Outline platelets.
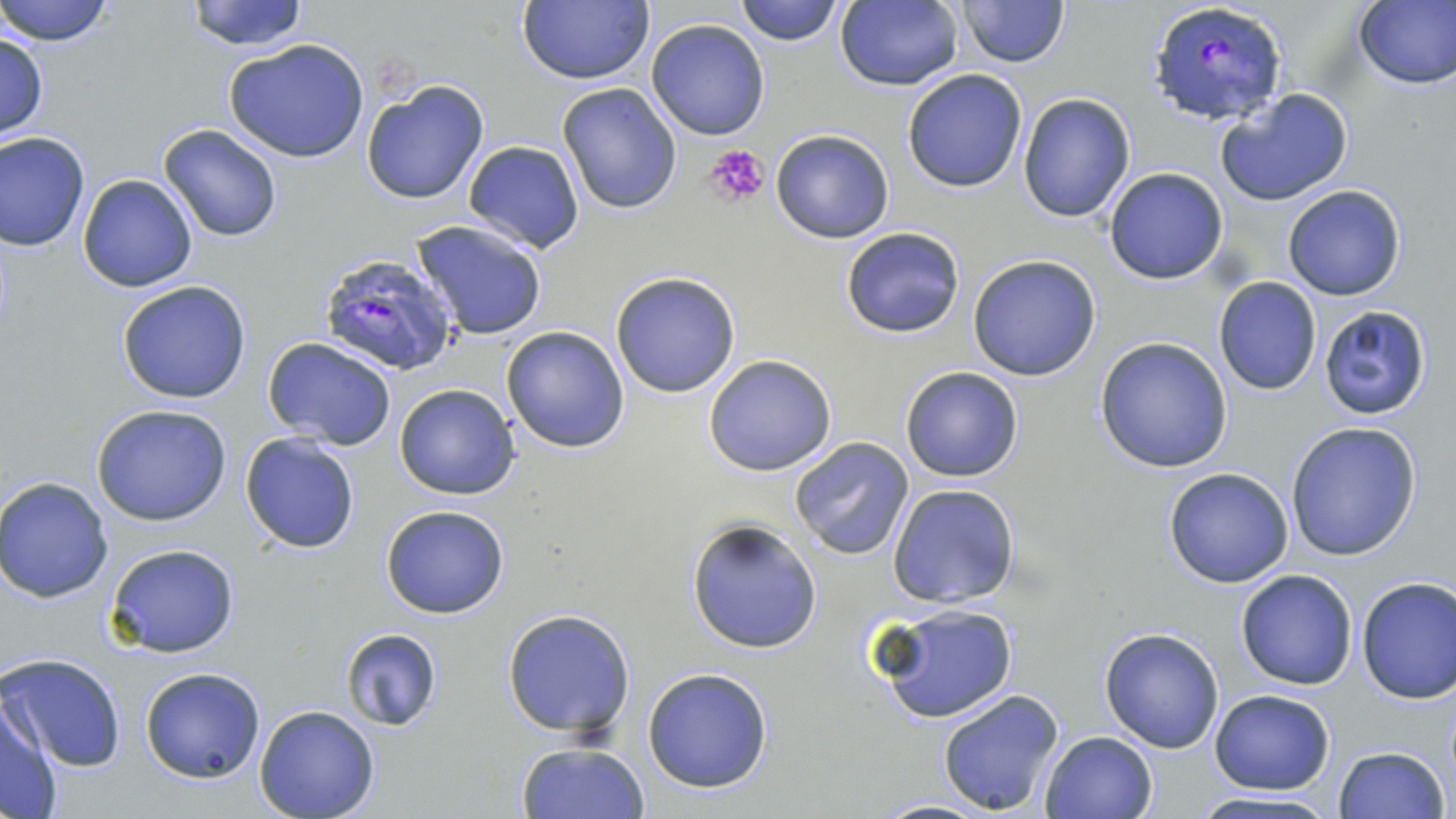

Approximate bounding boxes as [x1, y1, x2, y2] in pixels.
Platelets: [705, 143, 770, 208].

Summary:
  - Uninfected red blood cell locations: [0, 0, 117, 47], [186, 0, 310, 51], [520, 0, 655, 85], [732, 0, 846, 46], [835, 0, 964, 91], [956, 0, 1070, 68], [1353, 1, 1456, 90], [645, 19, 770, 140], [0, 32, 48, 142], [224, 38, 370, 163], [901, 68, 1028, 192], [360, 80, 489, 206], [556, 82, 684, 216], [1215, 88, 1355, 207], [1018, 92, 1136, 223], [158, 124, 283, 242], [769, 128, 895, 244], [1, 131, 90, 250], [462, 141, 585, 253], [1103, 166, 1228, 285], [78, 173, 198, 293], [1281, 184, 1406, 301], [411, 219, 549, 341], [840, 227, 966, 340], [967, 254, 1101, 381], [610, 272, 741, 398], [1213, 277, 1322, 396], [116, 280, 253, 404], [1317, 305, 1433, 421], [500, 325, 631, 455], [263, 336, 397, 450], [1094, 336, 1235, 472], [703, 354, 839, 476], [899, 365, 1024, 482], [394, 384, 520, 500], [91, 403, 232, 526], [1285, 420, 1423, 562], [240, 432, 362, 555], [789, 437, 914, 560], [1163, 467, 1296, 588], [0, 476, 114, 603], [888, 483, 1021, 609], [380, 503, 510, 619], [687, 519, 823, 655], [104, 542, 241, 659], [1236, 569, 1359, 690], [1356, 576, 1456, 705], [869, 600, 1019, 724], [502, 609, 636, 740], [336, 627, 446, 732], [1099, 627, 1225, 753], [2, 652, 127, 773], [139, 667, 266, 783], [642, 668, 774, 793], [937, 688, 1066, 816], [1209, 688, 1337, 795], [1, 696, 64, 817], [253, 704, 381, 819], [1041, 730, 1159, 819], [514, 742, 651, 819], [1332, 745, 1452, 819], [1186, 791, 1342, 819], [868, 799, 994, 818]
  - Plasmodium falciparum-infected red blood cell locations: [1147, 1, 1291, 128], [317, 250, 458, 376]
  - Slide-level diagnosis: Plasmodium falciparum
  - Preparation: thin blood film
  - Field of view: single
  - Image size: 1456×819 pixels
  - Modality: optical microscopy
  - Magnification: 1000x
  - Stain: May-Grünwald-Giemsa